Locate and identify every blood parasite.
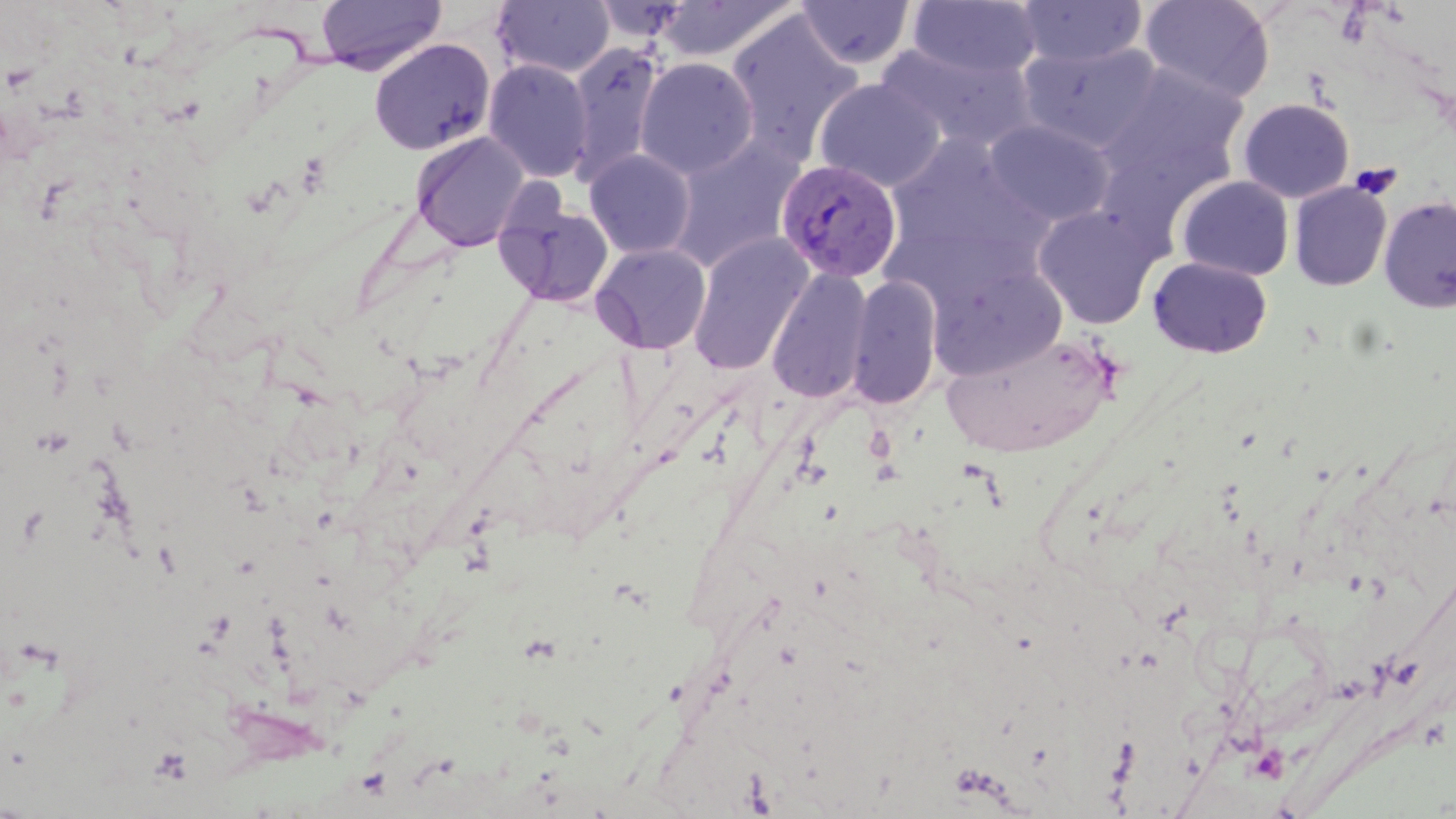
Approximate bounding boxes as [x1, y1, x2, y2] in pixels.
Plasmodium vivax-infected red blood cells: [777, 158, 903, 283].
No Plasmodium falciparum, Plasmodium ovale, Plasmodium malariae, Babesia divergens, or Trypanosoma brucei observed.

Platelet locations: [1350, 162, 1401, 199]. Uninfected red blood cell locations: [315, 0, 447, 75], [654, 0, 799, 63], [908, 0, 1043, 82], [1140, 0, 1275, 103], [492, 1, 615, 78], [797, 1, 915, 69], [1017, 1, 1147, 68], [725, 11, 863, 164], [369, 39, 496, 155], [878, 41, 1036, 153], [1019, 41, 1162, 152], [566, 42, 664, 185], [635, 57, 758, 179], [482, 59, 594, 183], [1101, 62, 1251, 185], [814, 78, 945, 191], [1238, 98, 1354, 202], [984, 119, 1114, 227], [410, 131, 530, 252], [668, 137, 806, 272], [883, 138, 1050, 293], [584, 149, 696, 258], [1177, 176, 1294, 281], [1290, 182, 1392, 291], [494, 193, 617, 309], [1379, 195, 1456, 313], [1033, 206, 1159, 328], [688, 232, 814, 375], [591, 242, 711, 355], [1148, 257, 1272, 358], [927, 262, 1069, 380], [767, 268, 871, 403], [846, 275, 942, 410], [941, 333, 1118, 457]. Slide-level diagnosis: Plasmodium vivax. Single field of view. Captured at 1000x magnification. Thin blood smear. May-Grünwald-Giemsa-stained preparation. Image is 1456×819 pixels. Light microscopy.